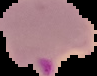
Summary:
  - Preparation: thin blood smear
  - Image type: segmented cell region on a black background
  - Result: Plasmodium parasites detected
  - Image size: 97×76 pixels